Classify this cell by malaria status.
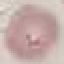

Uninfected.

Summary:
  - Stain: Giemsa
  - Preparation: thin smear
  - Capture: smartphone through the microscope eyepiece
  - Image type: automatically extracted cell patch, resized to 64 × 64 pixels